Locate every blood parasite and identify its species.
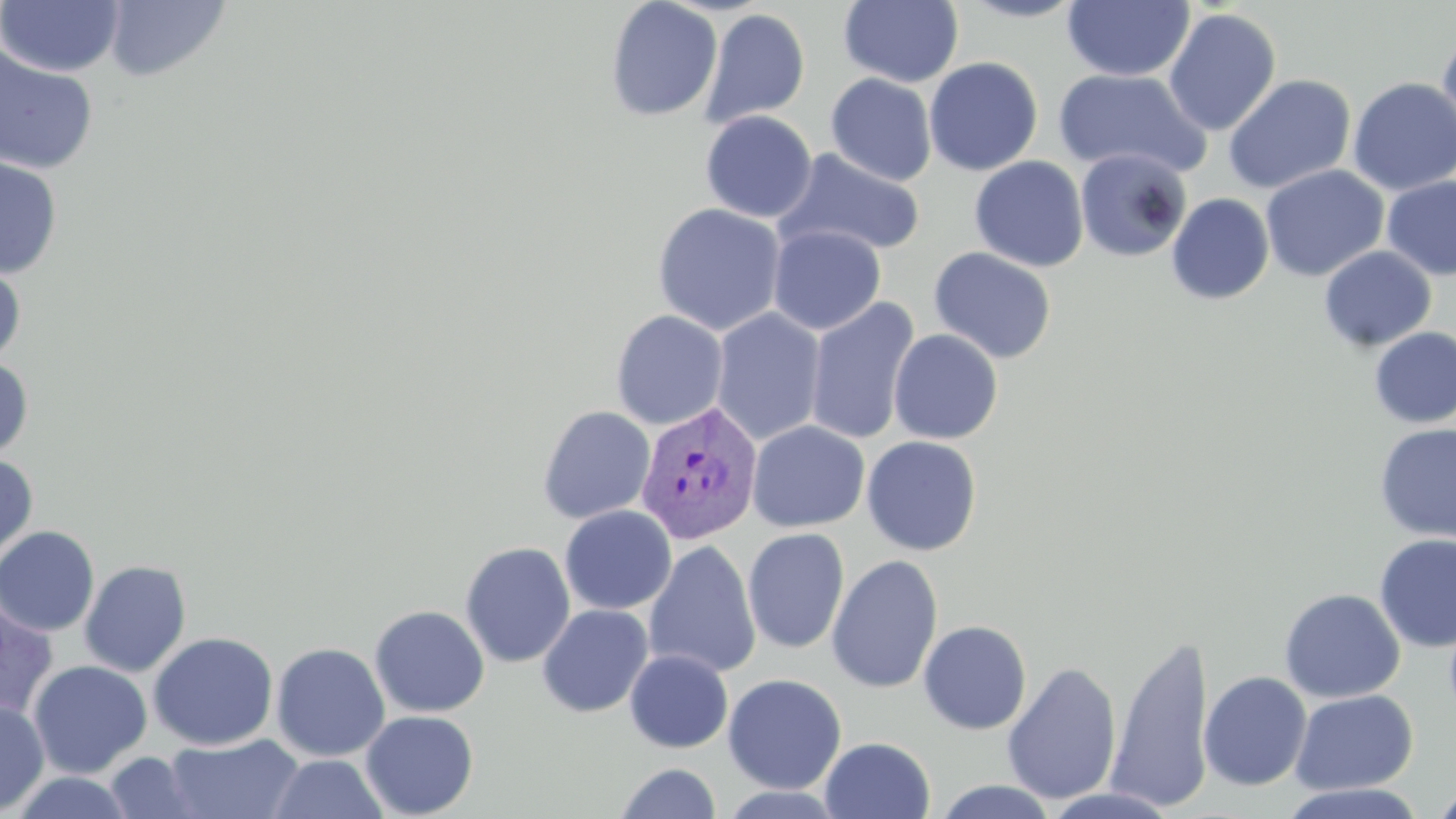
Approximate bounding boxes as (x1,y1)-(x2,y2) corner pairs in pixels.
Plasmodium vivax-infected red blood cells: (635,401)-(764,545).
No Plasmodium falciparum, Plasmodium ovale, Plasmodium malariae, Babesia divergens, or Trypanosoma brucei observed.

Uninfected red blood cell locations: (0,0)-(125,77), (103,0)-(231,81), (955,0)-(1092,23), (1062,0)-(1195,82), (605,1)-(722,121), (838,1)-(964,88), (700,8)-(810,129), (1163,8)-(1282,136), (1437,27)-(1456,154), (0,44)-(98,175), (924,57)-(1044,176), (1053,68)-(1211,179), (825,73)-(937,186), (1221,73)-(1357,194), (1347,77)-(1456,196), (699,110)-(818,223), (774,148)-(926,258), (1075,148)-(1191,263), (0,155)-(62,278), (969,156)-(1089,272), (1260,165)-(1389,282), (1382,175)-(1456,282), (1167,192)-(1274,305), (652,203)-(787,336), (768,225)-(886,335), (1318,245)-(1437,352), (929,247)-(1057,364), (0,260)-(26,366), (805,296)-(920,445), (711,307)-(827,446), (610,309)-(729,430), (1369,326)-(1456,429), (888,329)-(1003,444), (0,356)-(34,461), (537,405)-(656,524), (747,420)-(870,533), (1374,423)-(1456,543), (861,435)-(983,555), (0,453)-(38,564), (559,505)-(677,615), (0,526)-(100,636), (742,528)-(850,654), (1374,533)-(1456,652), (643,539)-(761,679), (460,541)-(576,668), (827,554)-(944,694), (79,559)-(191,677), (1279,588)-(1406,703), (0,599)-(58,720), (369,604)-(490,717), (536,604)-(654,718), (918,620)-(1032,735), (148,631)-(279,751), (1108,631)-(1216,813), (271,642)-(390,761), (624,649)-(733,753), (28,660)-(152,779), (1002,662)-(1122,805), (1198,671)-(1312,791), (722,673)-(847,794), (1290,689)-(1419,795), (0,699)-(49,816), (360,710)-(479,818), (164,733)-(303,819), (819,736)-(935,819), (104,751)-(204,818), (267,753)-(391,818), (614,762)-(722,819), (7,771)-(138,818), (933,779)-(1059,818), (1276,782)-(1429,818), (717,786)-(849,818), (1040,787)-(1181,818), (1432,787)-(1456,818). Slide-level diagnosis: Plasmodium vivax. Single field of view. Optical microscopy. Thin blood film. 1000x magnification. May-Grünwald-Giemsa stain. Image is 1456×819 pixels.